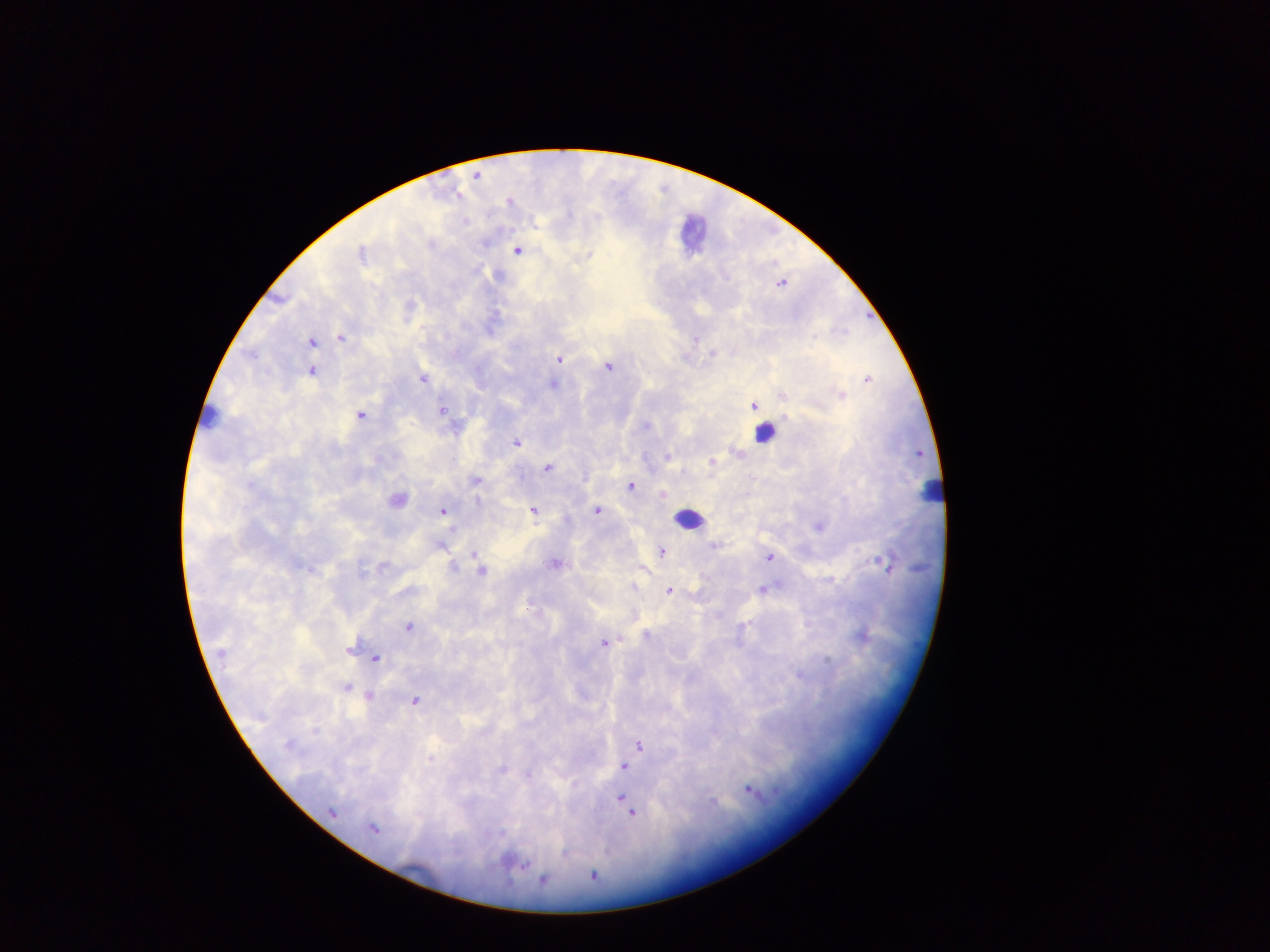

{
  "malaria_parasite_locations": "approximate centers as {x, y} in pixels: {475, 176}, {517, 251}, {361, 253}, {589, 255}, {341, 338}, {696, 339}, {311, 342}, {712, 353}, {558, 359}, {607, 367}, {311, 370}, {423, 379}, {867, 379}, {552, 384}, {841, 395}, {784, 396}, {753, 406}, {441, 411}, {361, 416}, {646, 425}, {516, 443}, {736, 452}, {667, 457}, {712, 462}, {546, 468}, {476, 481}, {631, 486}, {663, 494}, {397, 499}, {477, 502}, {443, 511}, {533, 511}, {597, 511}, {818, 527}, {440, 545}, {714, 546}, {662, 552}, {474, 554}, {769, 557}, {884, 563}, {555, 564}, {382, 566}, {453, 566}, {481, 571}, {633, 587}, {763, 589}, {669, 591}, {408, 627}, {647, 635}, {861, 637}, {604, 643}, {350, 650}, {221, 653}, {376, 658}, {830, 660}, {799, 675}, {346, 688}, {368, 697}, {416, 701}, {315, 730}, {640, 745}, {289, 746}, {431, 759}, {624, 766}, {502, 770}, {528, 775}, {749, 790}, {621, 797}, {714, 801}, {332, 812}, {631, 813}, {374, 829}, {522, 864}, {593, 876}, {543, 879}",
  "image_size": "1270×952 pixels",
  "object_labeled_both_malaria_parasite_and_leukocyte_by_the_source": "approximate centers as {x, y} in pixels: {764, 434}",
  "leukocyte_locations": "approximate centers as {x, y} in pixels: {691, 233}, {211, 417}, {930, 492}, {689, 519}",
  "capture": "mobile-phone photograph through a microscope",
  "country": "Ghana",
  "preparation": "thick blood smear",
  "field_of_view": "single"
}